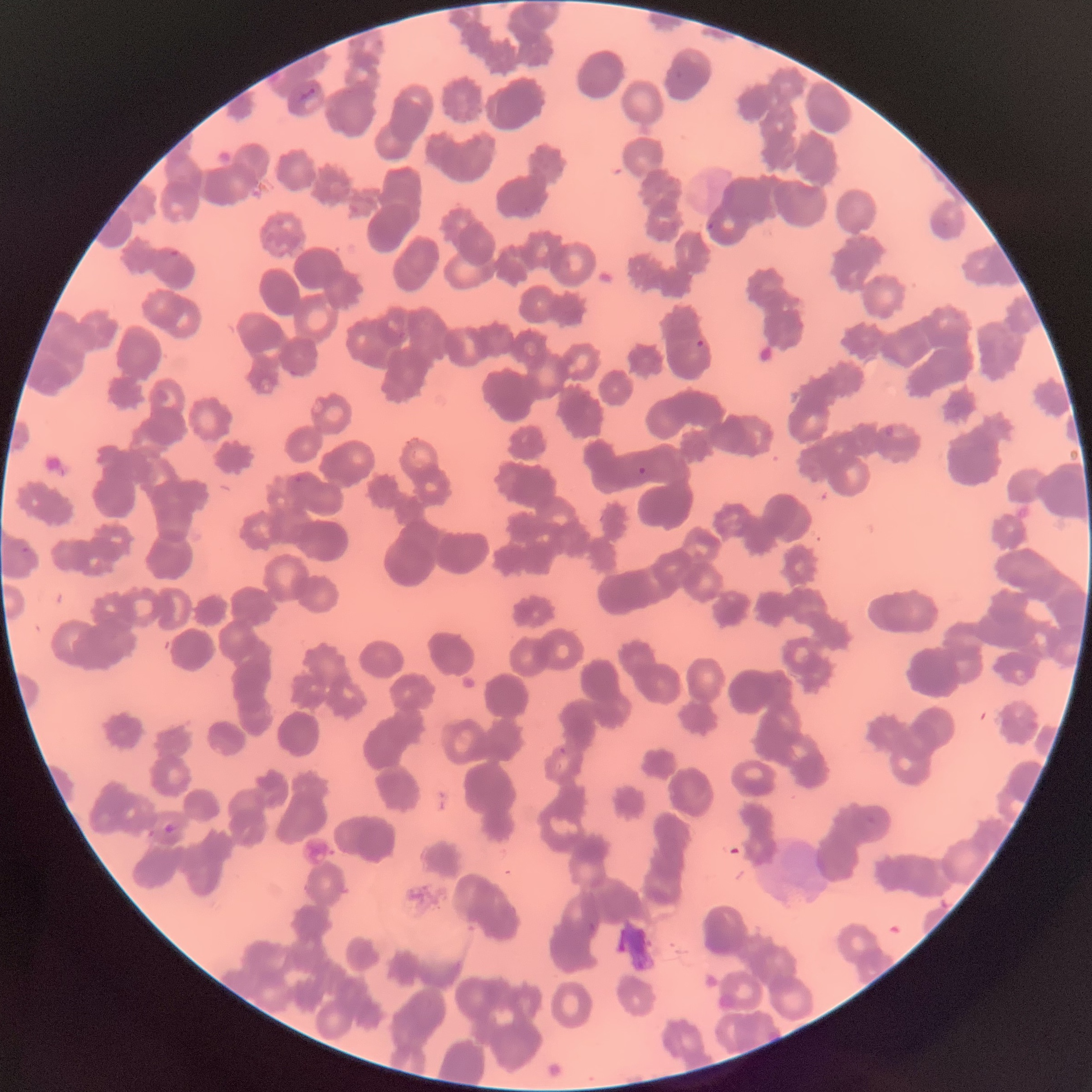

Summary:
  - Coordinate format: approximate bounding boxes as (x1, y1, x2, y2) in pixels
  - Plasmodium parasite locations: (299, 88, 317, 100), (706, 222, 715, 231), (696, 339, 705, 349), (636, 466, 648, 476), (162, 823, 178, 833)
  - Image size: 1092×1092 pixels
  - Preparation: thin blood smear
  - Modality: light microscopy
  - Red blood cell morphology: rouleaux formation